Locate every blood parasite and identify its species.
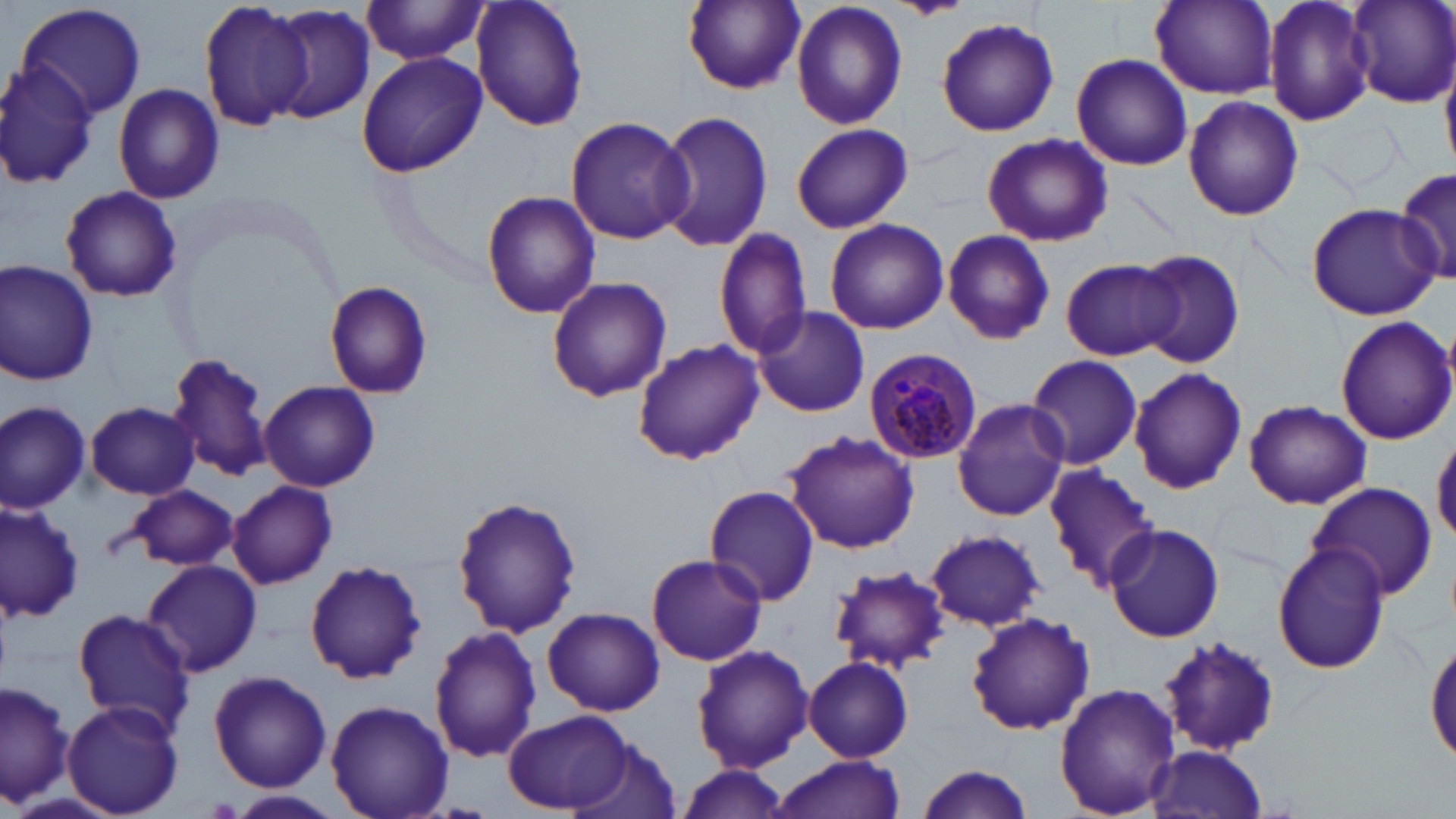
Approximate bounding boxes as [x1, y1, x2, y2] in pixels.
Plasmodium malariae-infected red blood cells: [863, 348, 982, 461].
No Plasmodium falciparum, Plasmodium ovale, Plasmodium vivax, Babesia divergens, or Trypanosoma brucei observed.

Uninfected red blood cell locations: [197, 0, 319, 132], [470, 0, 589, 132], [682, 0, 806, 92], [886, 0, 973, 20], [1150, 0, 1278, 98], [1261, 0, 1378, 126], [1349, 0, 1456, 107], [790, 1, 907, 130], [15, 2, 149, 123], [361, 2, 490, 66], [266, 5, 376, 124], [935, 16, 1060, 137], [355, 52, 487, 177], [1071, 53, 1193, 172], [0, 61, 100, 190], [113, 82, 226, 205], [1183, 96, 1304, 221], [656, 110, 773, 253], [566, 116, 693, 245], [791, 123, 912, 233], [982, 133, 1113, 248], [1393, 168, 1456, 284], [59, 186, 183, 302], [480, 190, 601, 320], [1305, 203, 1440, 319], [824, 217, 948, 333], [715, 227, 814, 360], [941, 229, 1055, 345], [1130, 248, 1246, 370], [1061, 258, 1179, 361], [0, 259, 100, 387], [547, 276, 672, 402], [323, 280, 433, 399], [751, 307, 870, 418], [1333, 316, 1455, 445], [632, 340, 766, 466], [167, 352, 273, 481], [1025, 353, 1143, 472], [1128, 367, 1247, 496], [259, 380, 380, 492], [953, 397, 1069, 522], [1244, 399, 1372, 510], [0, 401, 91, 512], [86, 403, 198, 499], [784, 431, 920, 554], [1432, 435, 1456, 546], [1044, 463, 1162, 592], [1307, 480, 1436, 602], [227, 481, 337, 589], [703, 483, 820, 605], [127, 484, 239, 571], [452, 495, 583, 637], [0, 501, 84, 621], [1104, 523, 1224, 642], [925, 529, 1048, 631], [1272, 541, 1392, 674], [646, 554, 766, 666], [141, 560, 262, 677], [303, 560, 430, 683], [828, 565, 950, 675], [542, 607, 664, 716], [73, 608, 195, 733], [965, 611, 1094, 735], [428, 625, 543, 763], [1426, 634, 1456, 769], [1160, 636, 1282, 755], [691, 644, 813, 772], [804, 656, 914, 762], [208, 670, 332, 791], [1, 678, 74, 811], [1054, 682, 1180, 817], [62, 700, 185, 817], [325, 700, 455, 819], [505, 710, 635, 811], [576, 737, 683, 819], [1146, 745, 1269, 818], [772, 755, 905, 819], [914, 763, 1036, 819], [677, 765, 793, 816], [231, 791, 341, 817]. Slide-level diagnosis: Plasmodium malariae. One field of a larger specimen. Light microscopy. Captured at 1000x magnification. Image is 1456×819 pixels. May-Grünwald-Giemsa stain. Thin blood film.